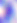 Photomicrograph. Toxoplasma gondii is seen. 400x magnification.